Classify this cell by malaria status.
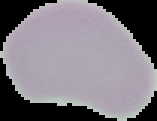
Uninfected.

Segmented cell region on a black background. From a thin blood film. Image is 157×121 pixels.